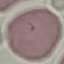
Summary:
  - Malaria status: uninfected
  - Capture: smartphone through the microscope eyepiece
  - Preparation: thin smear
  - Image type: automatically extracted cell patch, resized to 64 × 64 pixels
  - Stain: Giemsa